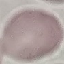

Result: no malaria parasites detected. Acquired by smartphone through the microscope eyepiece. Thin blood film. Automatically extracted cell patch, resized to 64 × 64 pixels. Giemsa stain.